Assess for Plasmodium parasites.
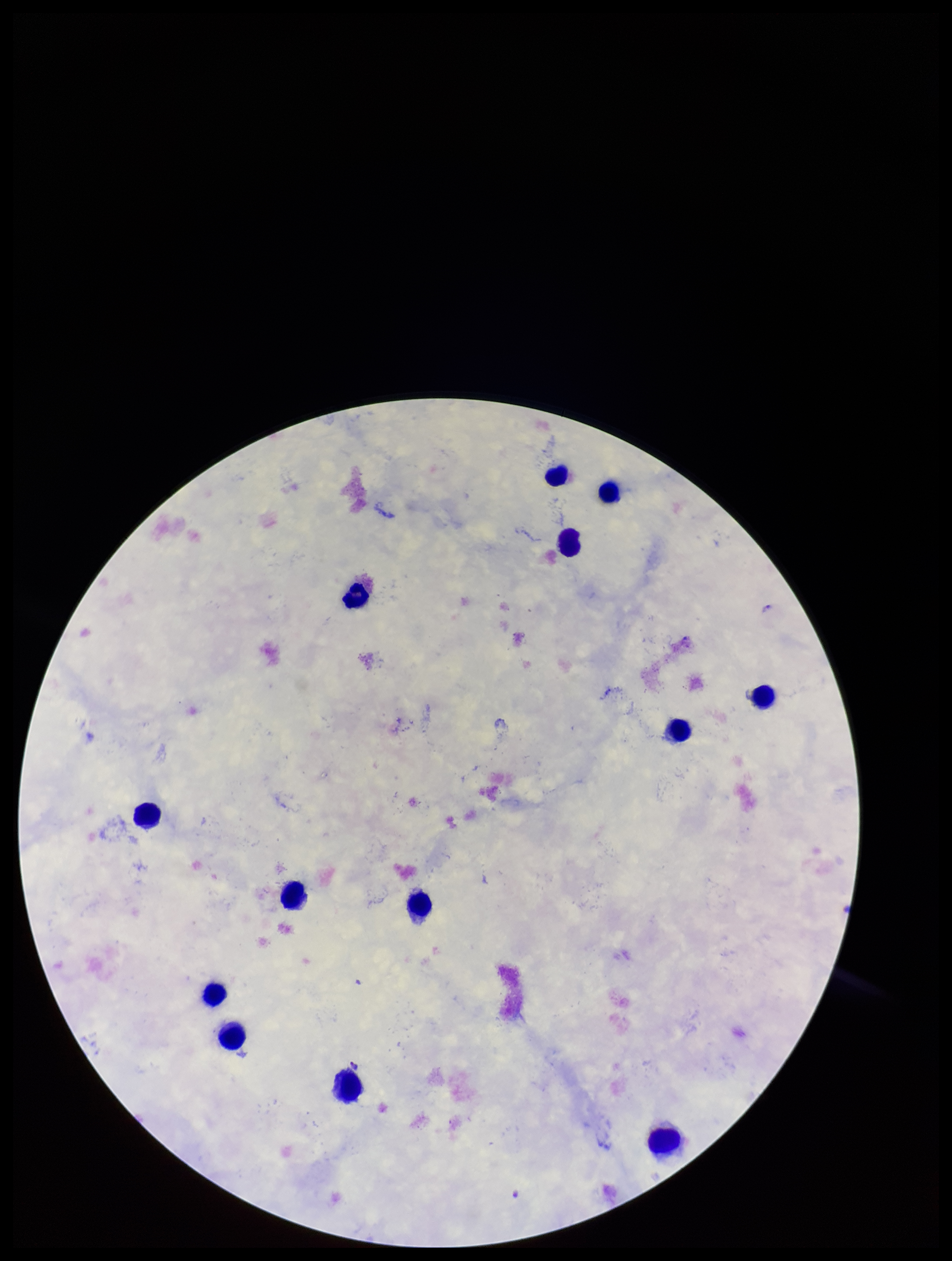

None identified.

Summary:
  - Species reported for this patient: Plasmodium falciparum
  - Parasite count: 0
  - Preparation: thick smear
  - Patient malaria status: infected
  - Image size: 952×1261 pixels
  - Leukocyte count: 13
  - Capture: smartphone photograph through the microscope eyepiece
  - Field of view: single
  - Stain: Giemsa